Name the parasite shown.
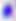
Toxoplasma gondii.

Summary:
  - Magnification: 400x
  - Modality: micrograph